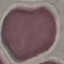

Malaria status: uninfected. Thin blood smear. Giemsa-stained preparation. Cell patch, automatically extracted from a larger field of view and resized to 64 × 64 pixels. Acquired by smartphone through the microscope eyepiece.